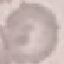

Malaria status: uninfected. Cell patch, automatically extracted from a larger field of view and resized to 64 × 64 pixels. Acquired by smartphone through the microscope eyepiece. Thin blood smear. Giemsa-stained preparation.